Locate every Plasmodium parasite.
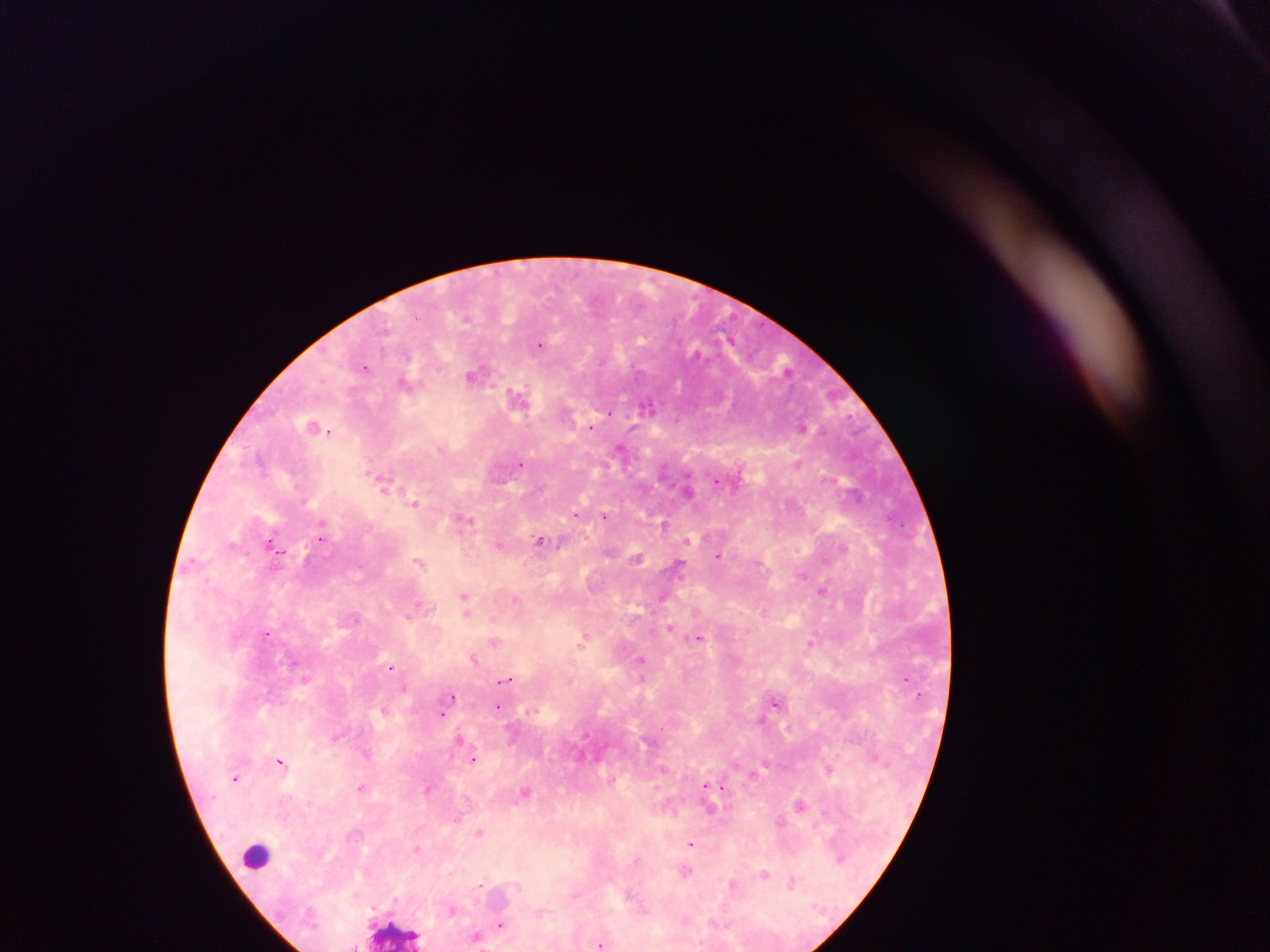

Approximate centers as {x, y} in pixels.
Plasmodium parasites: {468, 318}, {540, 345}, {696, 353}, {602, 360}, {365, 367}, {474, 375}, {407, 383}, {517, 398}, {646, 406}, {610, 413}, {314, 425}, {802, 426}, {590, 427}, {328, 430}, {620, 448}, {442, 449}, {521, 462}, {798, 462}, {717, 481}, {383, 482}, {688, 490}, {414, 502}, {577, 515}, {605, 516}, {465, 519}, {664, 524}, {322, 537}, {540, 541}, {272, 543}, {500, 544}, {843, 547}, {719, 555}, {637, 558}, {418, 561}, {679, 565}, {803, 575}, {823, 591}, {465, 597}, {662, 598}, {516, 600}, {418, 606}, {467, 611}, {764, 611}, {355, 619}, {670, 628}, {267, 633}, {698, 638}, {585, 639}, {495, 641}, {810, 642}, {474, 658}, {641, 660}, {390, 668}, {505, 680}, {405, 688}, {452, 697}, {775, 702}, {499, 706}, {384, 709}, {441, 714}, {761, 720}, {661, 728}, {336, 737}, {460, 739}, {366, 753}, {474, 759}, {280, 761}, {664, 768}, {830, 769}, {236, 778}, {707, 786}, {362, 787}, {719, 787}, {427, 790}, {525, 791}, {800, 804}, {712, 809}, {825, 813}, {457, 818}, {780, 822}, {479, 831}, {691, 843}, {416, 849}, {840, 858}, {636, 860}, {686, 871}, {764, 873}, {793, 883}, {480, 884}, {733, 884}, {452, 910}, {500, 925}, {477, 936}, {602, 945}, {354, 947}.

Leukocyte locations: {257, 855}, {395, 932}. Photographed through a microscope with a mobile-phone camera. Image is 1270×952 pixels. Thick blood smear. Sample from Ghana. Single field of view.